Classify this cell by malaria status.
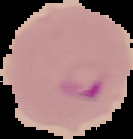
It is parasitized.

Segmented cell region on a black background. Image is 133×139 pixels. From a thin blood film.